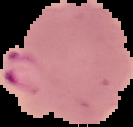

Summary:
  - Image type: segmented cell region with the area outside set to black
  - Image size: 133×127 pixels
  - Malaria status: parasitized
  - Preparation: thin blood smear